Give a bounding box for every leukocyte visible.
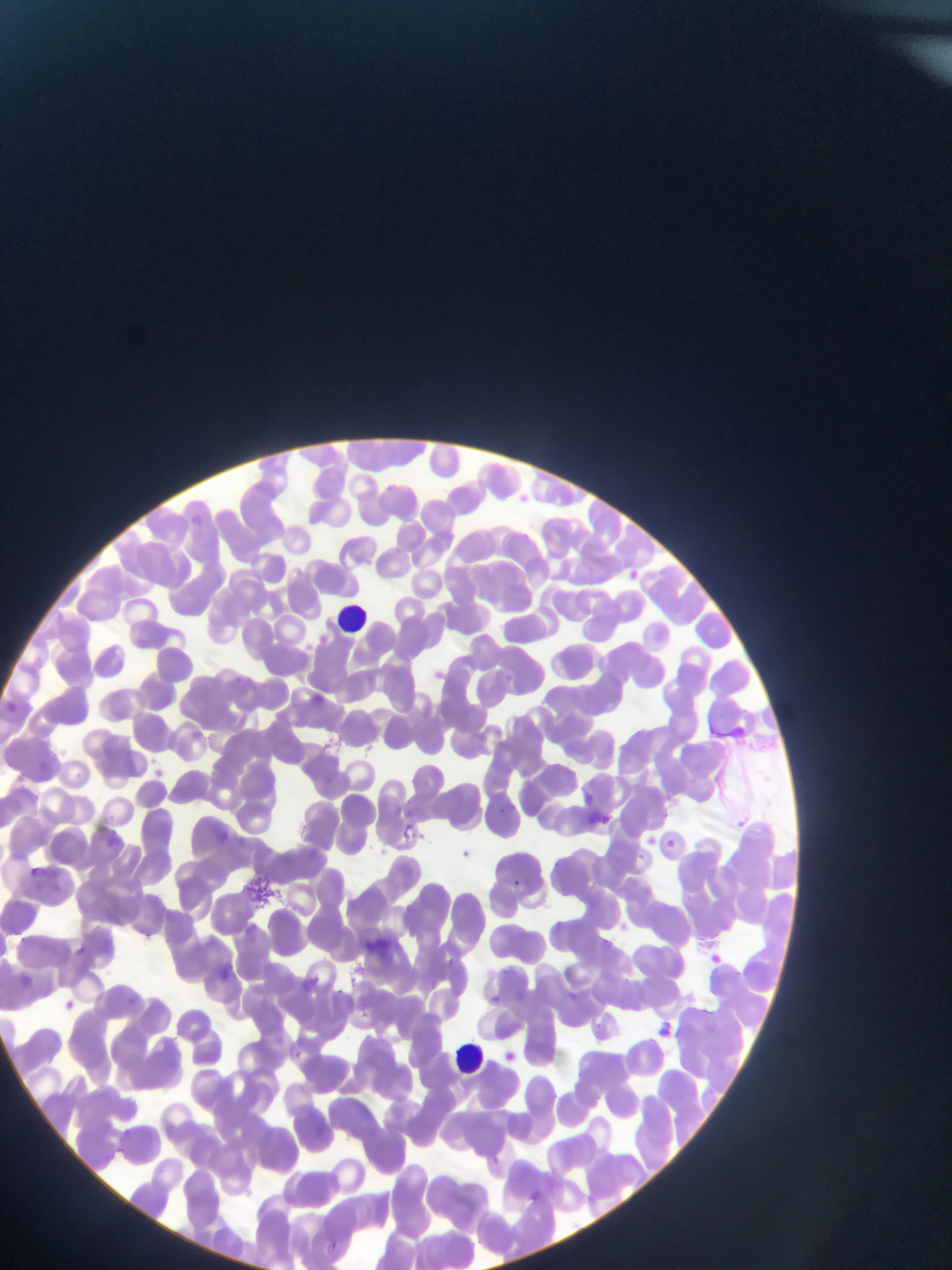

Approximate bounding boxes as {left, top, right, bottom} in pixels.
Leukocytes: {340, 603, 365, 635}, {449, 1041, 493, 1075}.

Plasmodium parasite locations: {624, 567, 644, 585}, {315, 632, 330, 646}, {232, 675, 249, 688}, {310, 692, 327, 708}, {501, 801, 519, 817}, {103, 813, 119, 828}, {730, 815, 751, 834}, {398, 823, 421, 845}, {212, 831, 232, 847}, {663, 836, 679, 851}, {457, 847, 474, 862}, {22, 864, 45, 883}, {509, 877, 523, 890}, {145, 932, 156, 942}, {16, 936, 26, 942}, {704, 949, 723, 967}, {213, 965, 233, 984}, {336, 988, 348, 998}, {486, 992, 504, 1008}, {60, 998, 78, 1015}, {359, 1010, 369, 1020}, {591, 1019, 603, 1033}, {654, 1020, 676, 1040}, {290, 1049, 305, 1062}, {499, 1050, 517, 1066}. Artifact (stain precipitate or debris) locations: {721, 720, 752, 739}, {246, 868, 281, 905}, {367, 923, 408, 960}. Thin blood film. Image is 952×1270 pixels. Single field of view. Sample from Ghana. Photographed through a microscope with a mobile-phone camera.